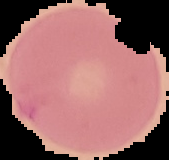

Summary:
  - Image size: 169×160 pixels
  - Preparation: thin blood smear
  - Malaria status: uninfected
  - Image type: cell region segmented out of the field of view; surrounding area masked to black